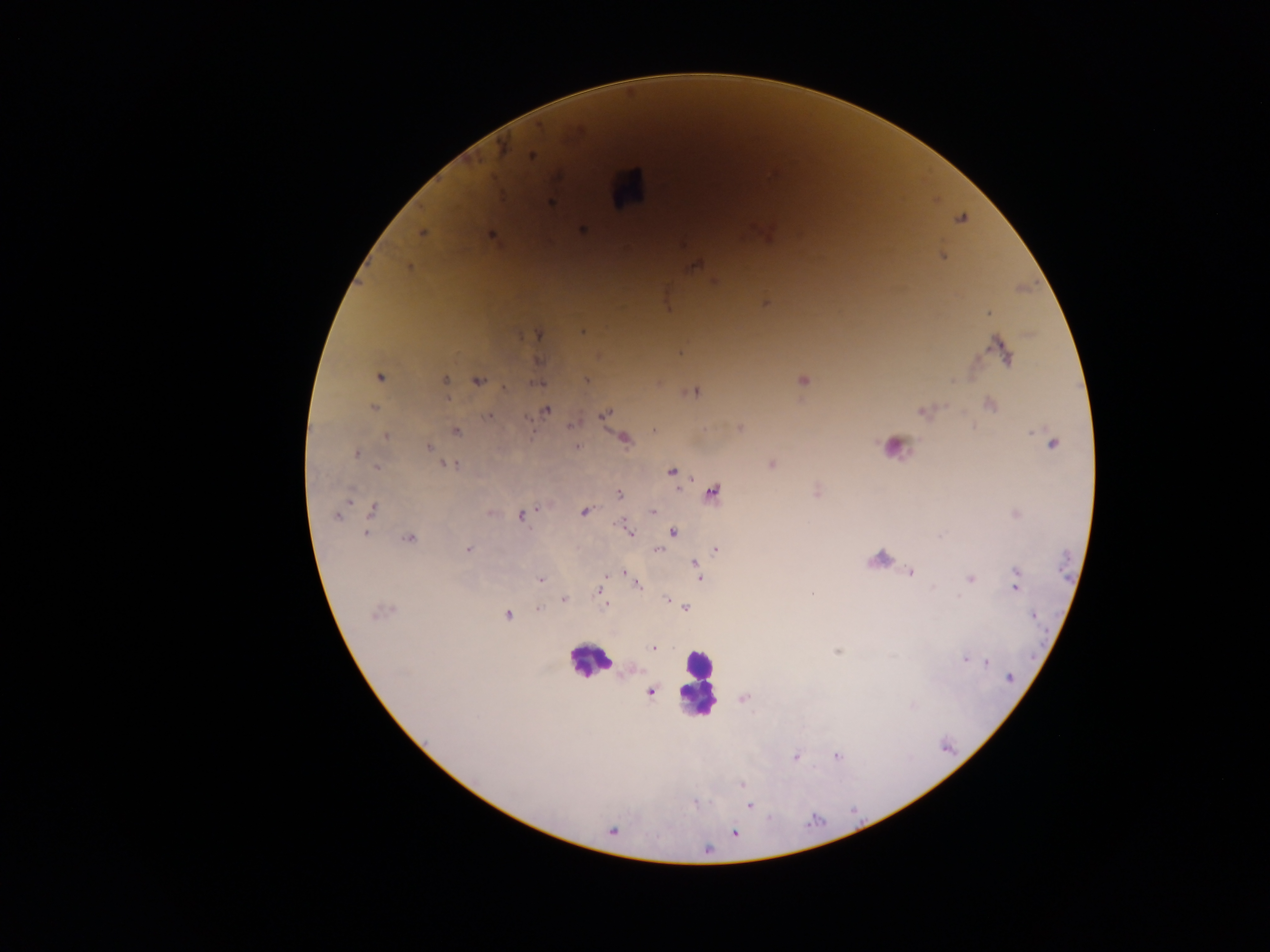

capture: mobile-phone photograph through a microscope
preparation: thick blood smear
plasmodium_parasite_locations: 'approximate centers as x y in pixels: 503 149; 532 157; 551 203; 583 230; 422 232; 491 236; 942 256; 695 265; 409 267; 715 282; 765 302; 989 313; 582 332; 538 335; 997 347; 1003 353; 539 361; 379 377; 586 380; 803 380; 445 381; 477 381; 537 381; 504 388; 695 392; 990 405; 374 407; 546 410; 922 413; 604 414; 488 416; 573 424; 740 428; 653 429; 456 431; 386 436; 624 438; 1052 444; 429 446; 576 446; 356 454; 772 464; 450 465; 378 468; 672 472; 713 492; 619 494; 373 511; 584 511; 491 513; 653 513; 336 516; 522 516; 630 532; 673 532; 366 534; 409 539; 468 549; 716 549; 658 550; 695 563; 624 572; 910 573; 700 578; 541 579; 971 579; 638 586; 933 587; 1015 588; 600 590; 959 597; 564 600; 667 600; 605 605; 686 608; 539 609; 379 613; 507 615; 653 648; 837 651; 965 660; 987 662; 1009 677; 651 692; 743 699; 838 756; 795 757; 742 784; 694 803; 750 806; 735 833; 708 849'
image_size: 1270×952 pixels
leukocyte_locations: 'approximate centers as x y in pixels: 626 187; 893 444; 883 555; 588 660; 698 684'
field_of_view: single
country: Ghana